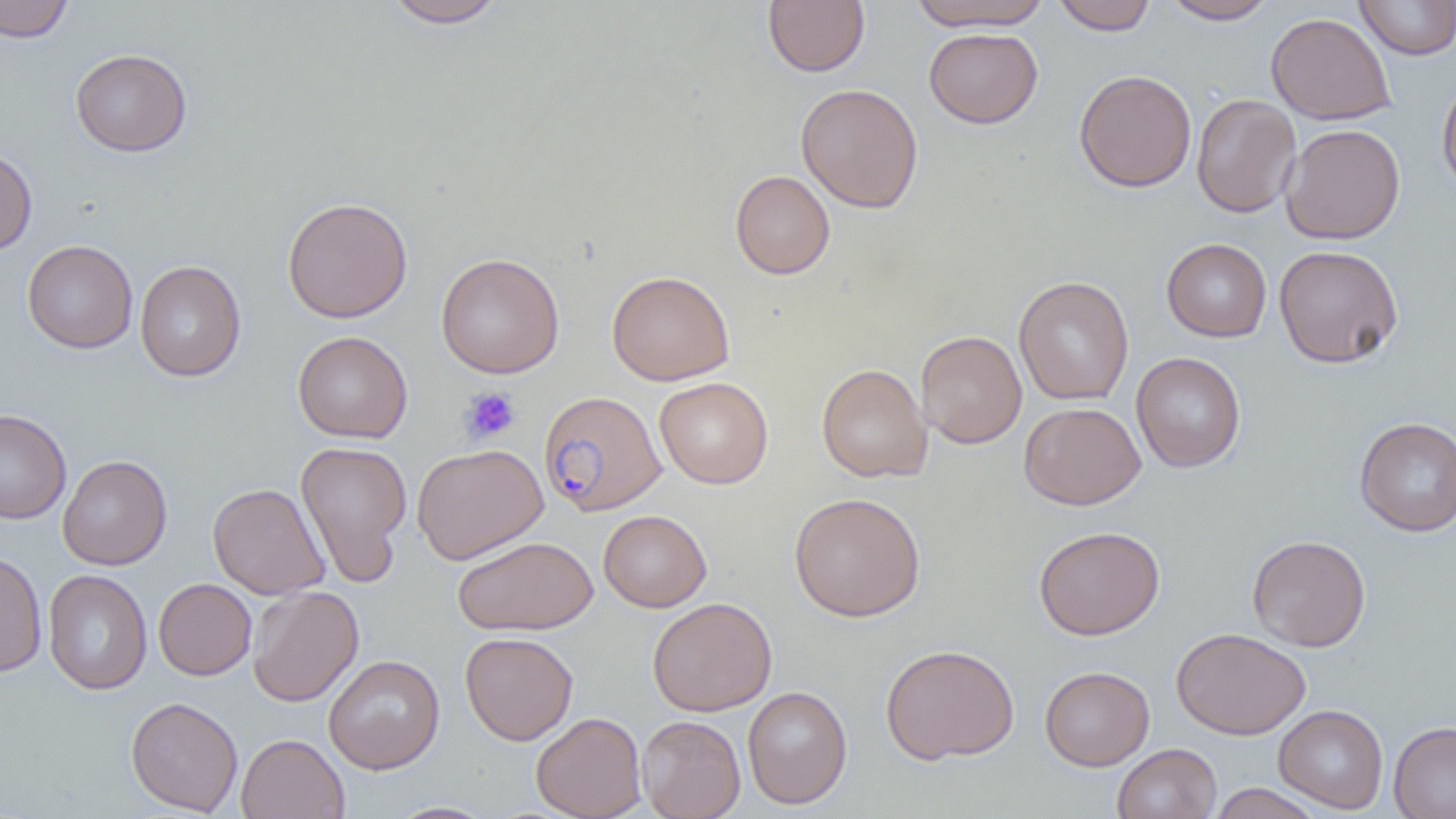

Summary:
  - Coordinate format: approximate bounding boxes as [x1, y1, x2, y2] in pixels
  - Uninfected red blood cell locations: [0, 0, 74, 43], [382, 0, 508, 28], [907, 0, 1053, 32], [1161, 0, 1278, 24], [1354, 0, 1456, 60], [762, 1, 870, 76], [1050, 1, 1158, 35], [1265, 12, 1396, 125], [924, 28, 1042, 128], [70, 48, 192, 156], [1074, 69, 1197, 193], [1437, 74, 1456, 200], [795, 83, 924, 214], [1191, 93, 1301, 218], [1280, 124, 1406, 244], [0, 144, 37, 256], [730, 170, 835, 280], [282, 196, 413, 324], [1161, 238, 1272, 342], [22, 240, 138, 354], [1273, 244, 1404, 368], [436, 253, 564, 378], [134, 260, 246, 381], [606, 270, 735, 386], [1013, 275, 1134, 405], [293, 330, 413, 443], [915, 330, 1027, 448], [1131, 352, 1246, 473], [816, 363, 932, 483], [654, 377, 773, 489], [1019, 402, 1146, 510], [0, 408, 71, 524], [1354, 416, 1456, 536], [295, 440, 412, 585], [411, 443, 548, 564], [58, 455, 172, 570], [208, 482, 329, 599], [788, 491, 926, 622], [598, 509, 711, 612], [1034, 525, 1165, 640], [1247, 534, 1371, 652], [452, 536, 599, 635], [0, 549, 48, 677], [42, 569, 153, 696], [153, 578, 256, 680], [247, 585, 364, 707], [647, 597, 777, 717], [1171, 627, 1311, 739], [460, 632, 578, 745], [880, 642, 1019, 765], [323, 654, 445, 774], [1040, 666, 1154, 770], [742, 686, 852, 809], [126, 696, 243, 815], [1273, 704, 1389, 814], [531, 712, 646, 818], [637, 715, 745, 819], [1388, 721, 1456, 818], [236, 733, 349, 819], [1112, 743, 1221, 819], [1207, 783, 1326, 818], [385, 801, 499, 819]
  - Plasmodium falciparum-infected red blood cell locations: [539, 391, 667, 516]
  - Platelet locations: [459, 386, 522, 445]
  - Slide-level diagnosis: Plasmodium falciparum
  - Magnification: 1000x
  - Preparation: thin blood smear
  - Modality: light microscopy
  - Field of view: single
  - Image size: 1456×819 pixels